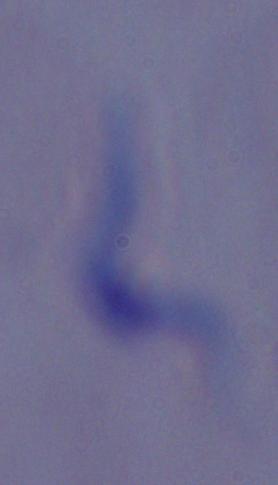

Summary:
  - Identification: trypanosome
  - Modality: micrograph
  - Magnification: 1000x